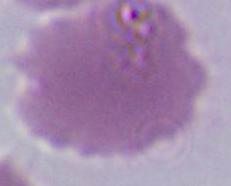
A red blood cell is shown. Micrograph. 1000x magnification.